Outline each blood parasite and name the species.
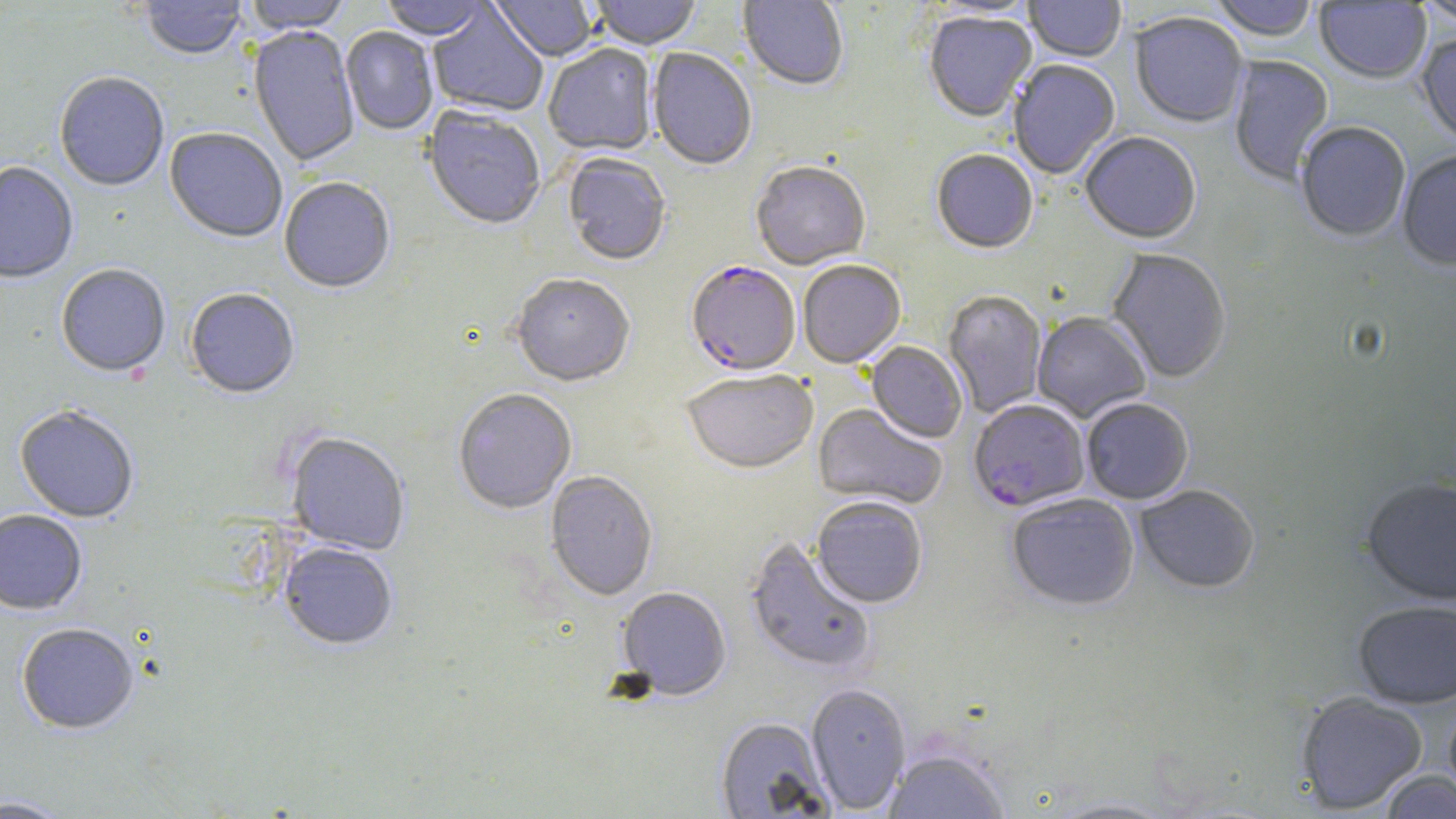
Approximate bounding boxes as [x1, y1, x2, y2] in pixels.
Plasmodium falciparum-infected red blood cells: [686, 264, 801, 378], [968, 400, 1089, 513].
No Plasmodium ovale, Plasmodium malariae, Plasmodium vivax, Babesia divergens, or Trypanosoma brucei observed.

Summary:
  - Uninfected red blood cell locations: [140, 0, 247, 61], [243, 0, 351, 36], [380, 0, 488, 42], [489, 0, 598, 62], [589, 0, 702, 52], [737, 0, 848, 92], [924, 0, 1039, 19], [1024, 0, 1126, 63], [1210, 0, 1318, 44], [1416, 0, 1456, 28], [1315, 2, 1431, 85], [427, 4, 547, 118], [924, 13, 1037, 124], [1130, 14, 1248, 129], [248, 26, 360, 168], [340, 27, 438, 136], [1416, 34, 1456, 149], [544, 46, 657, 158], [647, 50, 756, 171], [1228, 56, 1334, 187], [1008, 61, 1121, 180], [54, 73, 169, 193], [422, 108, 546, 232], [1296, 123, 1411, 244], [165, 129, 287, 245], [1080, 134, 1201, 246], [931, 151, 1038, 255], [1398, 152, 1456, 273], [563, 154, 671, 268], [0, 163, 78, 285], [751, 163, 870, 272], [279, 179, 396, 296], [1106, 250, 1231, 384], [798, 261, 906, 369], [56, 265, 170, 378], [511, 276, 634, 389], [185, 289, 300, 400], [943, 291, 1048, 417], [1032, 313, 1150, 423], [866, 342, 967, 444], [681, 371, 818, 477], [453, 390, 577, 516], [1081, 400, 1194, 505], [812, 404, 946, 510], [14, 406, 139, 524], [286, 434, 409, 557], [545, 472, 658, 602], [1361, 478, 1456, 607], [1135, 486, 1260, 596], [1006, 495, 1139, 612], [810, 498, 928, 610], [0, 511, 87, 616], [745, 539, 877, 677], [279, 543, 397, 651], [617, 588, 731, 702], [1352, 602, 1456, 710], [17, 624, 139, 736], [806, 684, 911, 814], [1296, 692, 1428, 815], [1443, 698, 1456, 807], [715, 718, 833, 818], [883, 750, 1010, 819], [1378, 770, 1456, 818], [0, 796, 74, 818], [1044, 797, 1182, 818]
  - Slide-level diagnosis: Plasmodium falciparum
  - Magnification: 1000x
  - Modality: optical microscopy
  - Preparation: thin blood smear
  - Stain: May-Grünwald-Giemsa
  - Field of view: one of a larger specimen
  - Image size: 1456×819 pixels